Identify the parasite.
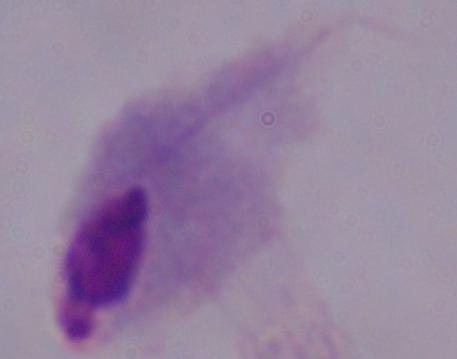
A trichomonad.

1000x magnification. Photomicrograph.